Locate every uninfected red blood cell.
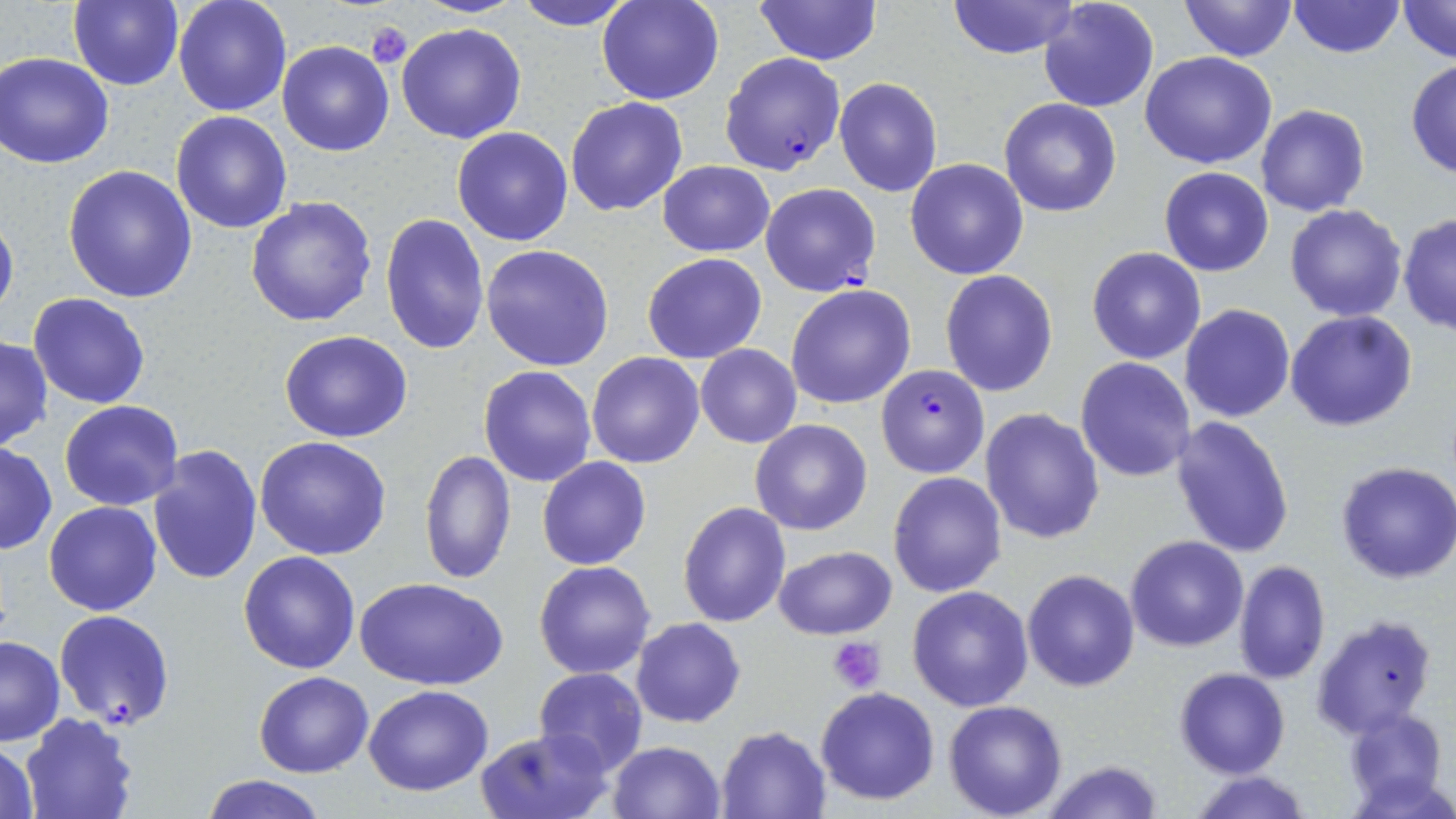

Approximate bounding boxes as (x1, y1, x2, y2) in pixels.
Uninfected red blood cells: (172, 0, 292, 116), (510, 0, 640, 29), (598, 0, 724, 105), (755, 0, 881, 65), (946, 0, 1080, 59), (1038, 0, 1159, 114), (1179, 0, 1295, 61), (1396, 0, 1455, 66), (66, 1, 185, 89), (1288, 1, 1404, 58), (396, 22, 526, 145), (277, 40, 394, 156), (2, 52, 116, 168), (1140, 52, 1278, 170), (1406, 60, 1456, 182), (833, 77, 943, 198), (566, 97, 688, 217), (1000, 99, 1121, 218), (1258, 104, 1369, 217), (170, 110, 292, 232), (451, 126, 574, 247), (905, 157, 1030, 280), (658, 161, 774, 257), (64, 165, 199, 303), (1159, 167, 1273, 276), (245, 196, 377, 327), (1284, 202, 1408, 323), (0, 206, 19, 328), (381, 213, 490, 356), (1398, 213, 1456, 335), (481, 243, 615, 371), (1086, 246, 1207, 364), (642, 252, 766, 363), (939, 271, 1058, 397), (786, 283, 916, 410), (27, 292, 152, 409), (1180, 304, 1295, 423), (1286, 310, 1418, 431), (280, 330, 412, 442), (0, 337, 52, 451), (695, 343, 802, 448), (587, 351, 706, 469), (1075, 357, 1195, 482), (479, 365, 597, 485), (59, 400, 183, 510), (981, 408, 1106, 544), (1168, 416, 1295, 558), (749, 419, 872, 536), (255, 436, 393, 560), (0, 443, 55, 555), (147, 445, 263, 586), (419, 449, 515, 585), (537, 457, 650, 569), (1334, 460, 1456, 584), (887, 471, 1007, 597), (678, 500, 791, 628), (45, 501, 162, 617), (1125, 535, 1249, 652), (772, 546, 898, 639), (238, 551, 361, 674), (534, 560, 655, 678), (1234, 561, 1330, 684), (1022, 568, 1140, 693), (356, 575, 508, 690), (907, 586, 1034, 711), (1311, 614, 1438, 740), (631, 618, 745, 728), (0, 635, 65, 746), (1175, 667, 1291, 778), (533, 668, 647, 776), (254, 671, 373, 777), (364, 685, 493, 796), (815, 686, 941, 805), (943, 699, 1069, 818), (1343, 708, 1446, 810), (20, 710, 141, 819), (716, 725, 833, 817), (476, 729, 610, 819), (2, 741, 40, 819), (606, 741, 726, 819), (1039, 759, 1165, 818), (1188, 771, 1317, 819), (203, 774, 328, 819).

Summary:
  - Platelet locations: (366, 21, 412, 69), (829, 636, 888, 693)
  - Plasmodium falciparum-infected red blood cell locations: (719, 53, 846, 175), (761, 184, 881, 297), (876, 363, 989, 480), (54, 610, 175, 730)
  - Slide-level diagnosis: Plasmodium falciparum
  - Stain: May-Grünwald-Giemsa
  - Modality: optical microscopy
  - Magnification: 1000x
  - Preparation: thin blood film
  - Image size: 1456×819 pixels
  - Field of view: single